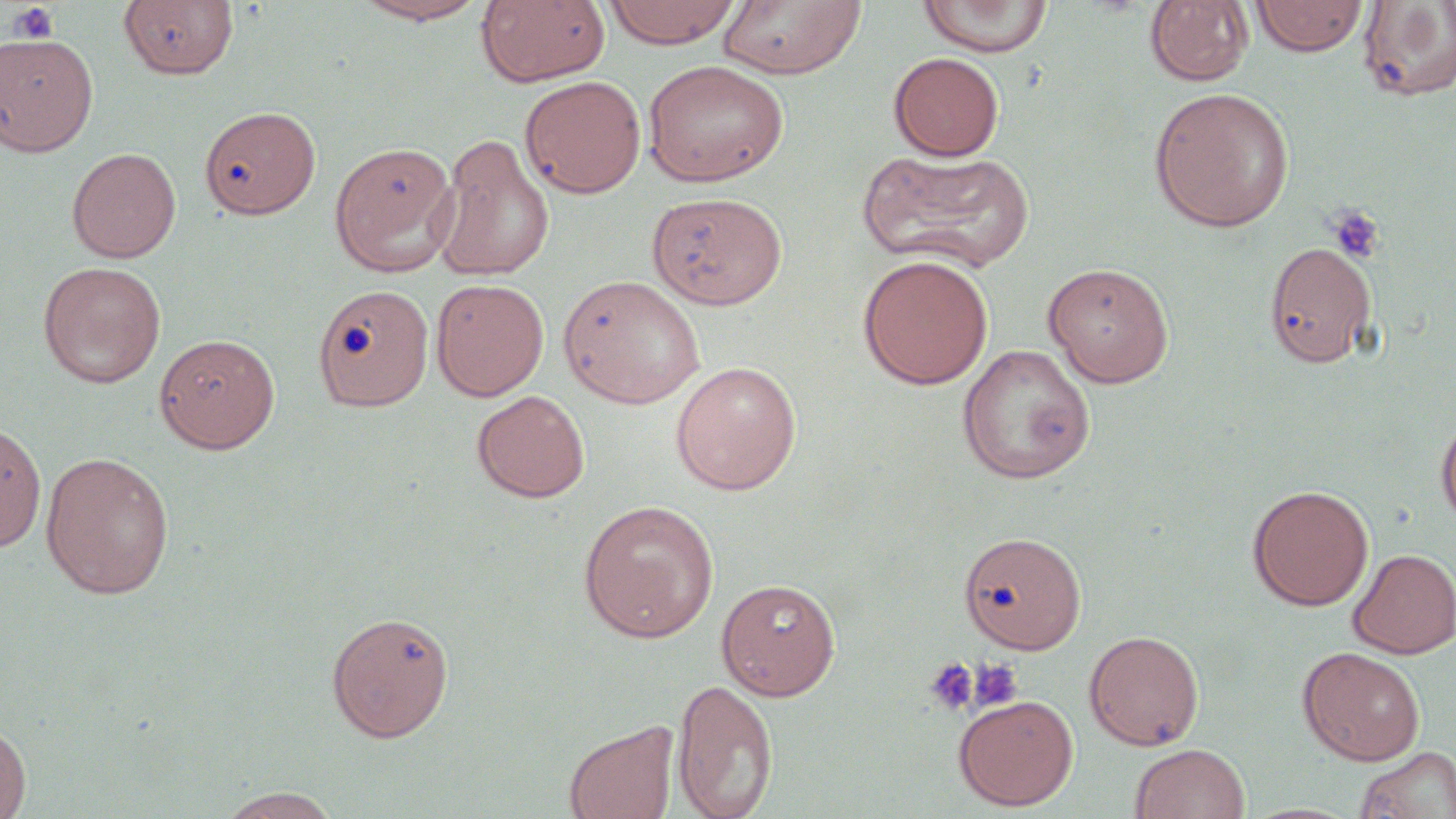

slide-level diagnosis = negative for blood parasites
platelet locations = approximate bounding boxes as [x1, y1, x2, y2] in pixels: [8, 3, 59, 44], [1325, 204, 1386, 264], [923, 657, 980, 716], [969, 658, 1024, 711]
uninfected red blood cell locations = approximate bounding boxes as [x1, y1, x2, y2] in pixels: [351, 0, 491, 25], [476, 0, 610, 87], [603, 0, 741, 48], [917, 0, 1055, 58], [1249, 0, 1370, 56], [118, 1, 239, 80], [716, 1, 867, 80], [1145, 1, 1253, 86], [1357, 1, 1456, 103], [0, 32, 99, 157], [888, 52, 1004, 161], [642, 59, 788, 187], [520, 76, 646, 198], [1149, 86, 1295, 233], [199, 104, 321, 219], [431, 134, 555, 282], [329, 141, 459, 276], [66, 147, 181, 263], [858, 149, 1035, 273], [647, 192, 787, 310], [1264, 240, 1378, 369], [857, 254, 994, 390], [37, 261, 166, 388], [1042, 261, 1175, 388], [557, 274, 706, 409], [430, 278, 549, 401], [313, 284, 434, 412], [155, 333, 281, 453], [955, 344, 1095, 484], [670, 360, 802, 495], [472, 390, 590, 503], [1436, 413, 1456, 530], [0, 421, 47, 552], [40, 451, 175, 600], [1247, 484, 1374, 611], [577, 499, 720, 643], [959, 531, 1086, 654], [1348, 548, 1456, 659], [717, 578, 841, 700], [325, 610, 454, 743], [1084, 629, 1204, 751], [1297, 646, 1425, 765], [672, 678, 778, 819], [953, 694, 1078, 811], [563, 719, 680, 819], [0, 720, 32, 819], [1129, 743, 1250, 819], [1352, 746, 1455, 819], [219, 787, 343, 818]
field of view = one of a larger specimen
stain = May-Grünwald-Giemsa
magnification = 1000x
preparation = thin blood film
image size = 1456×819 pixels
modality = light microscopy